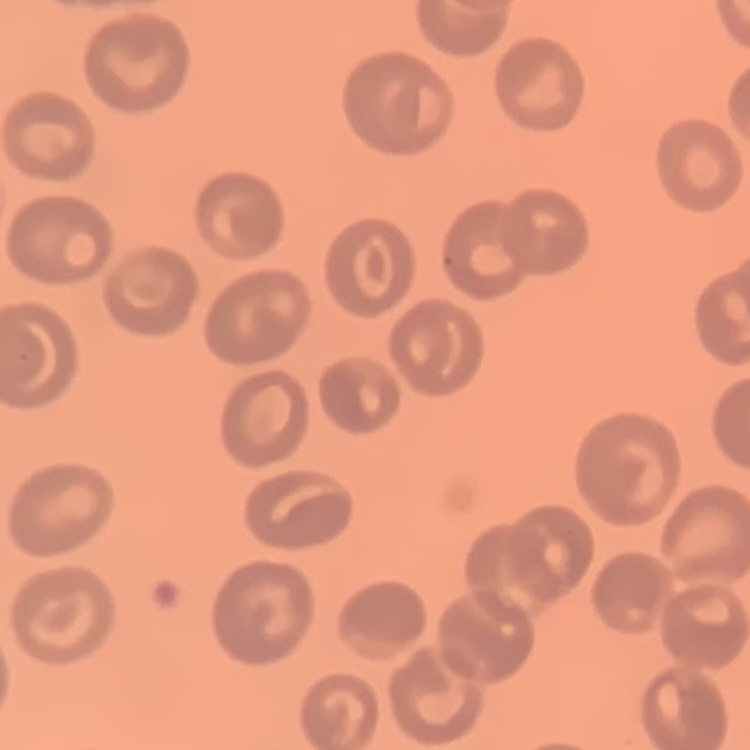
{
  "erythrocyte_morphology": "no rouleaux formation",
  "image_type": "one tile cut from a larger photomicrograph",
  "preparation": "thin peripheral smear",
  "stain": "Field's or Giemsa"
}